Outline each uninfected red blood cell.
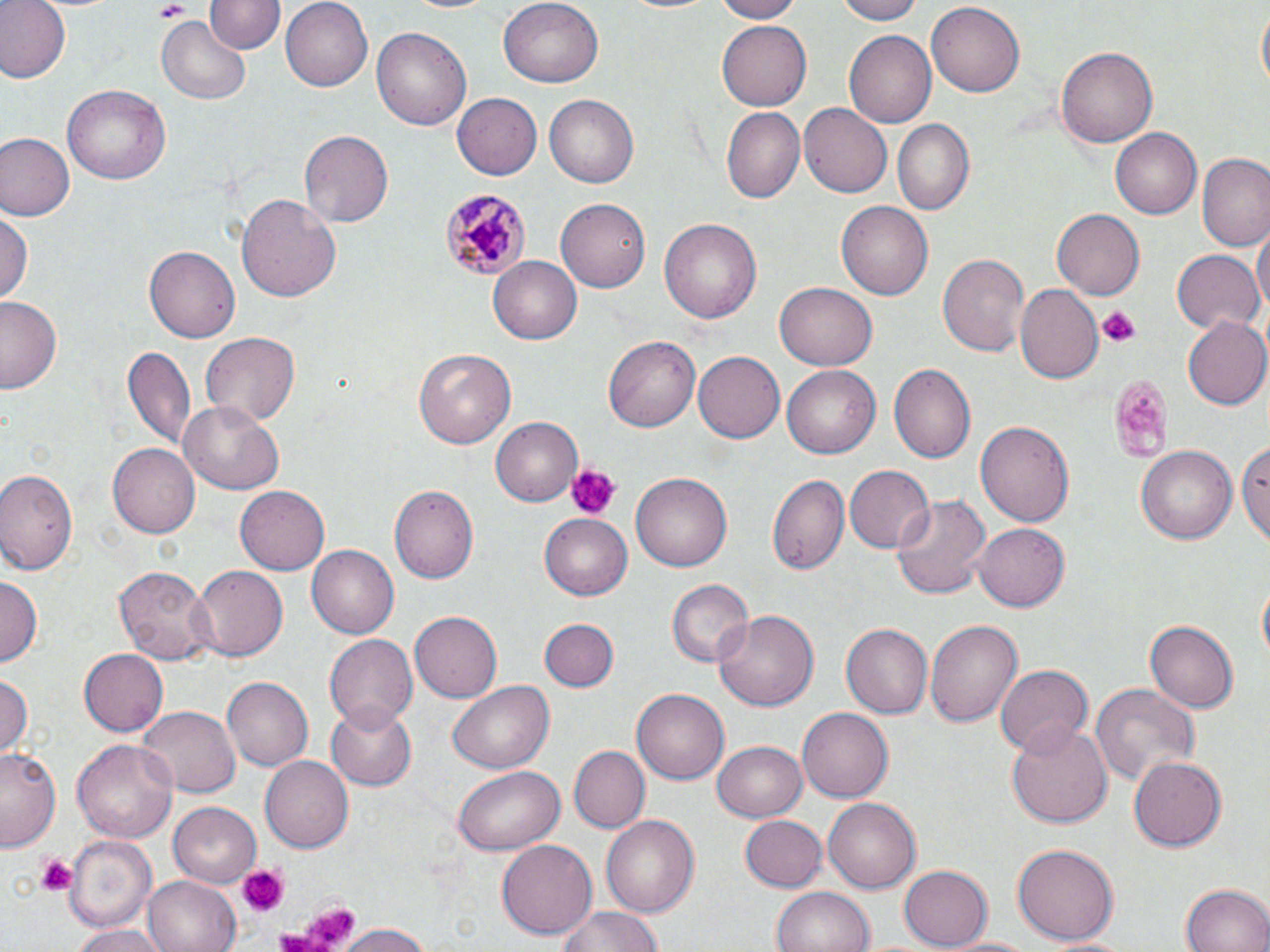
Approximate bounding boxes as named x1/y1/x2/y2 corners in pixels.
Uninfected red blood cells: (x1=0, y1=0, x2=68, y2=83), (x1=206, y1=0, x2=284, y2=55), (x1=279, y1=0, x2=372, y2=91), (x1=706, y1=0, x2=806, y2=22), (x1=835, y1=0, x2=926, y2=24), (x1=496, y1=1, x2=602, y2=88), (x1=1255, y1=1, x2=1269, y2=95), (x1=925, y1=4, x2=1025, y2=98), (x1=156, y1=17, x2=249, y2=105), (x1=717, y1=21, x2=812, y2=111), (x1=371, y1=23, x2=470, y2=128), (x1=846, y1=31, x2=935, y2=126), (x1=1056, y1=46, x2=1160, y2=148), (x1=63, y1=84, x2=169, y2=184), (x1=452, y1=93, x2=542, y2=180), (x1=542, y1=94, x2=640, y2=188), (x1=799, y1=104, x2=891, y2=199), (x1=721, y1=106, x2=804, y2=205), (x1=893, y1=119, x2=976, y2=217), (x1=1109, y1=128, x2=1199, y2=219), (x1=298, y1=130, x2=394, y2=229), (x1=0, y1=134, x2=75, y2=221), (x1=1199, y1=154, x2=1270, y2=252), (x1=234, y1=193, x2=342, y2=304), (x1=557, y1=196, x2=655, y2=292), (x1=836, y1=201, x2=932, y2=301), (x1=1052, y1=208, x2=1147, y2=300), (x1=1, y1=211, x2=32, y2=307), (x1=659, y1=217, x2=761, y2=324), (x1=1251, y1=220, x2=1269, y2=319), (x1=146, y1=244, x2=244, y2=341), (x1=1171, y1=250, x2=1262, y2=335), (x1=937, y1=253, x2=1031, y2=357), (x1=488, y1=256, x2=582, y2=345), (x1=774, y1=282, x2=877, y2=371), (x1=1014, y1=284, x2=1101, y2=383), (x1=0, y1=295, x2=64, y2=394), (x1=1182, y1=316, x2=1270, y2=410), (x1=199, y1=332, x2=299, y2=426), (x1=603, y1=337, x2=700, y2=432), (x1=122, y1=345, x2=194, y2=453), (x1=414, y1=348, x2=517, y2=449), (x1=692, y1=350, x2=784, y2=441), (x1=889, y1=364, x2=975, y2=463), (x1=782, y1=365, x2=879, y2=458), (x1=178, y1=398, x2=284, y2=494), (x1=489, y1=418, x2=581, y2=505), (x1=976, y1=420, x2=1074, y2=530), (x1=1235, y1=436, x2=1270, y2=544), (x1=106, y1=444, x2=199, y2=538), (x1=1136, y1=445, x2=1237, y2=545), (x1=846, y1=465, x2=934, y2=553), (x1=0, y1=469, x2=80, y2=576), (x1=631, y1=473, x2=731, y2=572), (x1=769, y1=476, x2=848, y2=574), (x1=234, y1=486, x2=329, y2=575), (x1=390, y1=486, x2=478, y2=585), (x1=892, y1=492, x2=991, y2=601), (x1=539, y1=516, x2=631, y2=599), (x1=974, y1=522, x2=1069, y2=611), (x1=307, y1=546, x2=399, y2=639), (x1=112, y1=564, x2=214, y2=664), (x1=188, y1=564, x2=290, y2=662), (x1=0, y1=575, x2=42, y2=663), (x1=1257, y1=577, x2=1269, y2=669), (x1=666, y1=580, x2=751, y2=669), (x1=716, y1=608, x2=819, y2=714), (x1=409, y1=611, x2=500, y2=702), (x1=539, y1=618, x2=618, y2=691), (x1=926, y1=618, x2=1024, y2=731), (x1=1144, y1=620, x2=1239, y2=711), (x1=841, y1=622, x2=934, y2=718), (x1=325, y1=632, x2=417, y2=728), (x1=78, y1=647, x2=168, y2=735), (x1=994, y1=665, x2=1090, y2=757), (x1=0, y1=673, x2=33, y2=755), (x1=221, y1=676, x2=312, y2=771), (x1=447, y1=679, x2=553, y2=774), (x1=1090, y1=682, x2=1201, y2=786), (x1=632, y1=687, x2=729, y2=784), (x1=327, y1=704, x2=416, y2=790), (x1=135, y1=706, x2=241, y2=798), (x1=798, y1=708, x2=892, y2=803), (x1=1005, y1=720, x2=1111, y2=829), (x1=71, y1=736, x2=179, y2=844), (x1=711, y1=738, x2=808, y2=822), (x1=567, y1=745, x2=649, y2=833), (x1=1, y1=747, x2=62, y2=851), (x1=1128, y1=755, x2=1226, y2=852), (x1=261, y1=756, x2=353, y2=853), (x1=452, y1=766, x2=566, y2=854), (x1=824, y1=797, x2=921, y2=894), (x1=168, y1=802, x2=262, y2=885), (x1=600, y1=814, x2=700, y2=919), (x1=740, y1=814, x2=827, y2=892), (x1=62, y1=834, x2=157, y2=931), (x1=497, y1=839, x2=596, y2=938), (x1=1012, y1=843, x2=1118, y2=945), (x1=899, y1=864, x2=994, y2=948), (x1=142, y1=875, x2=240, y2=952), (x1=1181, y1=884, x2=1269, y2=952), (x1=772, y1=888, x2=875, y2=952), (x1=551, y1=906, x2=667, y2=952), (x1=335, y1=921, x2=437, y2=952), (x1=69, y1=925, x2=169, y2=952), (x1=939, y1=936, x2=1049, y2=951).

Plasmodium malariae-infected red blood cell locations: (x1=435, y1=188, x2=530, y2=282). Platelet locations: (x1=153, y1=3, x2=191, y2=22), (x1=1097, y1=306, x2=1140, y2=347), (x1=1102, y1=372, x2=1175, y2=463), (x1=565, y1=462, x2=621, y2=520), (x1=34, y1=852, x2=79, y2=898), (x1=239, y1=865, x2=285, y2=915), (x1=288, y1=903, x2=359, y2=950), (x1=272, y1=924, x2=322, y2=952). Slide-level diagnosis: Plasmodium malariae. One field of a larger specimen. Image is 1270×952 pixels. May-Grünwald-Giemsa stain. Light microscopy. Thin blood film. 1000x magnification.